Assess this cell for malaria.
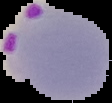
Parasitized.

Summary:
  - Image size: 112×103 pixels
  - Preparation: thin blood film
  - Image type: segmented cell region on a black background